Assess for malaria.
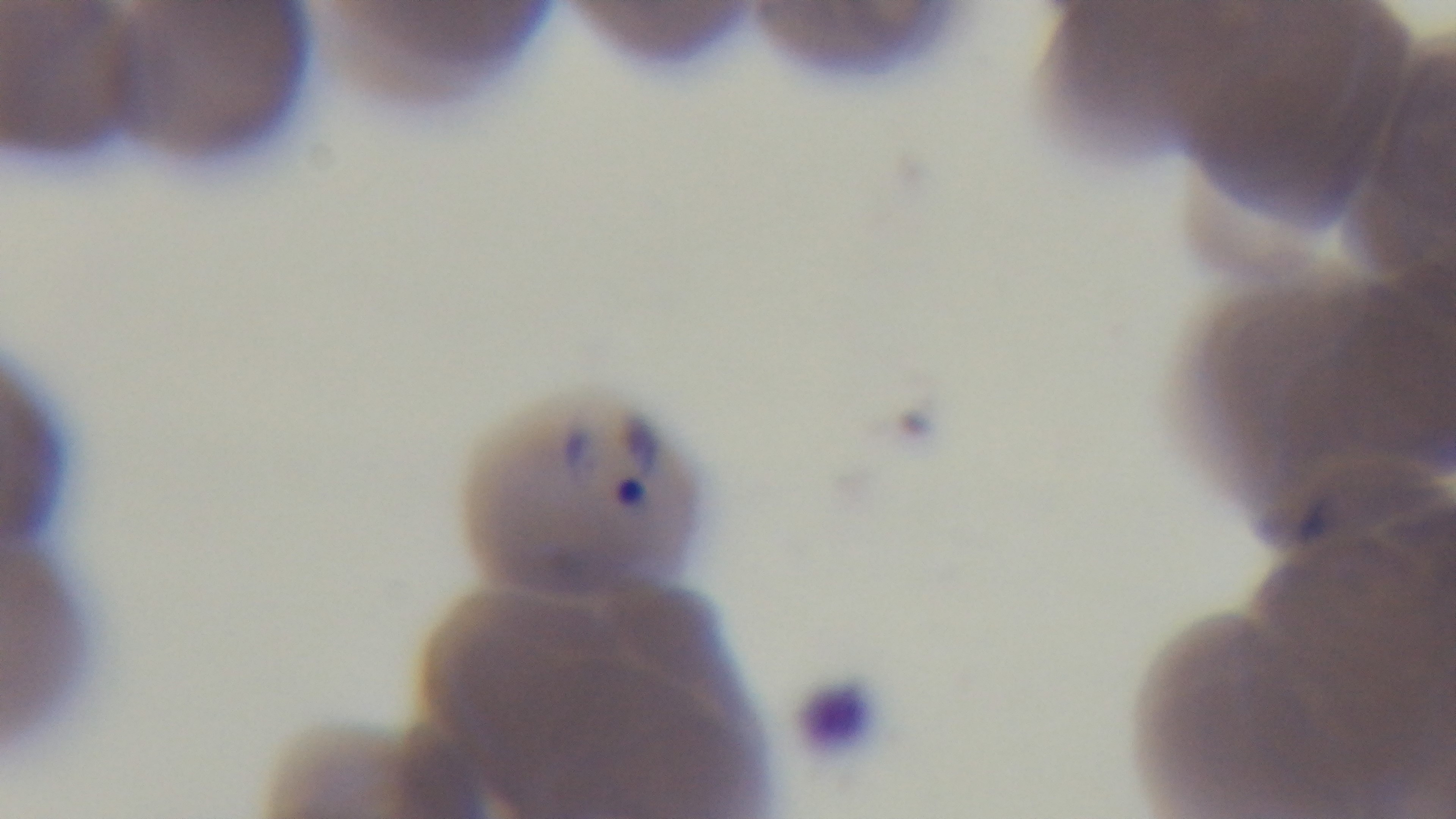

Infected.

capture: mounted 4K digital camera
objective: 100x oil immersion
modality: light microscopy
field_of_view: one from the slide
stain: Giemsa
preparation: thin smear